Assess this cell for malaria.
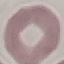
It is uninfected.

Summary:
  - Image type: automatically extracted cell patch, resized to 64 × 64 pixels
  - Stain: Giemsa
  - Capture: smartphone through the microscope eyepiece
  - Preparation: thin smear